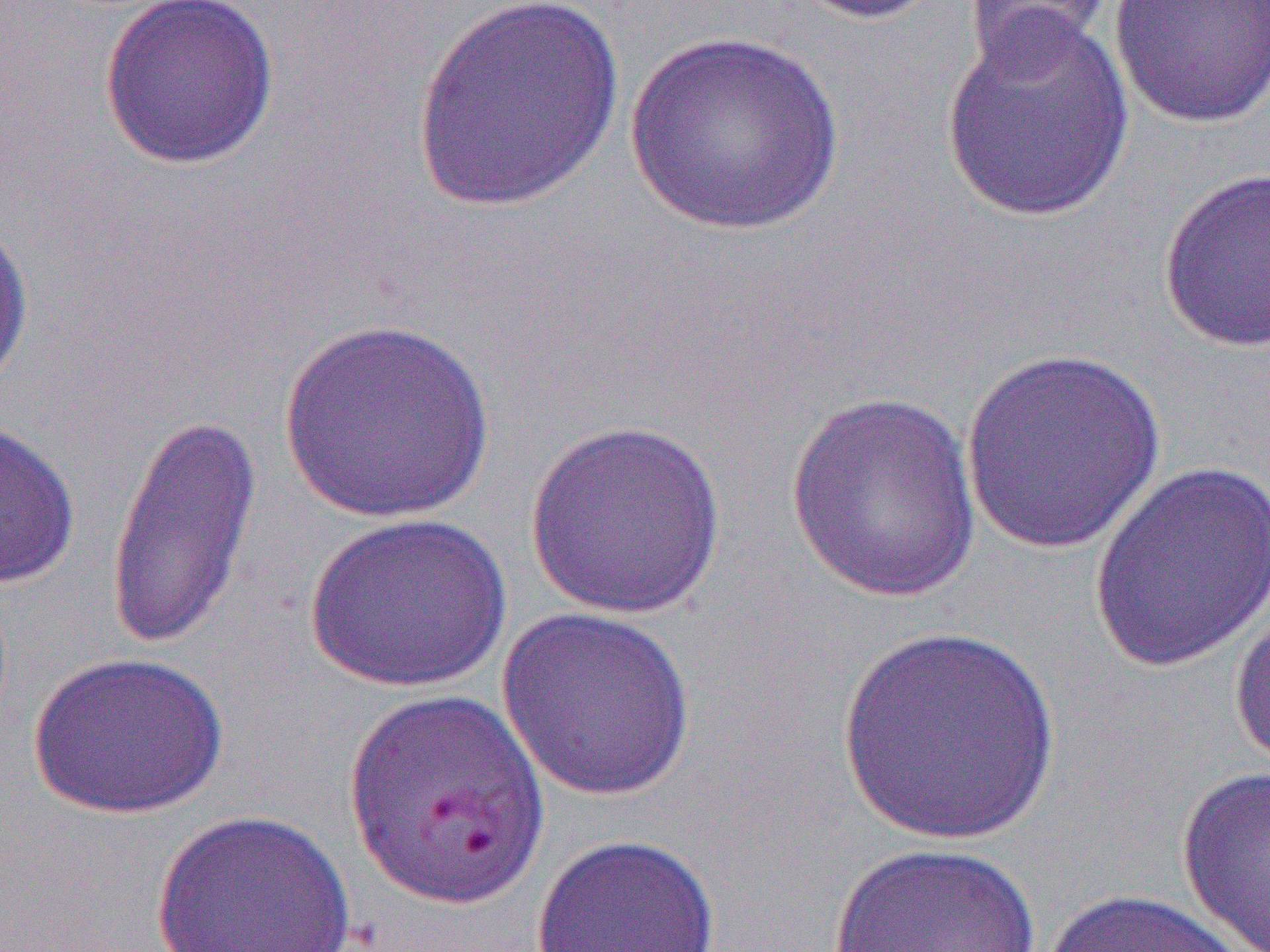
Summary:
  - Coordinate format: approximate bounding boxes as [x1, y1, x2, y2] in pixels
  - Uninfected red blood cell locations: [97, 0, 281, 171], [784, 0, 948, 26], [1109, 0, 1270, 129], [409, 1, 627, 216], [963, 1, 1114, 70], [940, 11, 1137, 226], [622, 31, 846, 237], [1157, 166, 1270, 354], [0, 215, 34, 402], [275, 317, 497, 525], [958, 348, 1168, 556], [784, 391, 983, 603], [103, 411, 263, 654], [0, 417, 81, 589], [523, 418, 729, 620], [1088, 461, 1270, 674], [302, 510, 514, 694], [1230, 596, 1270, 777], [496, 606, 697, 803], [834, 625, 1062, 846], [28, 651, 229, 818], [1176, 765, 1270, 950], [149, 808, 358, 952], [530, 833, 723, 952], [828, 842, 1044, 952], [1041, 887, 1257, 952]
  - Slide-level diagnosis: Plasmodium falciparum
  - Preparation: thin blood film
  - Image size: 1270×952 pixels
  - Modality: optical microscopy
  - Field of view: one of a larger specimen
  - Magnification: 1000x